Assess this cell for malaria.
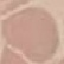
It is uninfected.

Summary:
  - Preparation: thin smear
  - Capture: smartphone through the microscope eyepiece
  - Image type: cell patch, automatically extracted from a larger field of view and resized to 64 × 64 pixels
  - Stain: Giemsa